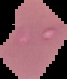

image size = 67×79 pixels
malaria status = parasitized
preparation = thin blood smear
image type = cell region segmented out of the field of view; surrounding area masked to black